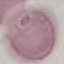

Summary:
  - Malaria status: uninfected
  - Preparation: thin smear
  - Stain: Giemsa
  - Image type: cell patch, automatically extracted from a larger field of view and resized to 64 × 64 pixels
  - Capture: smartphone through the microscope eyepiece